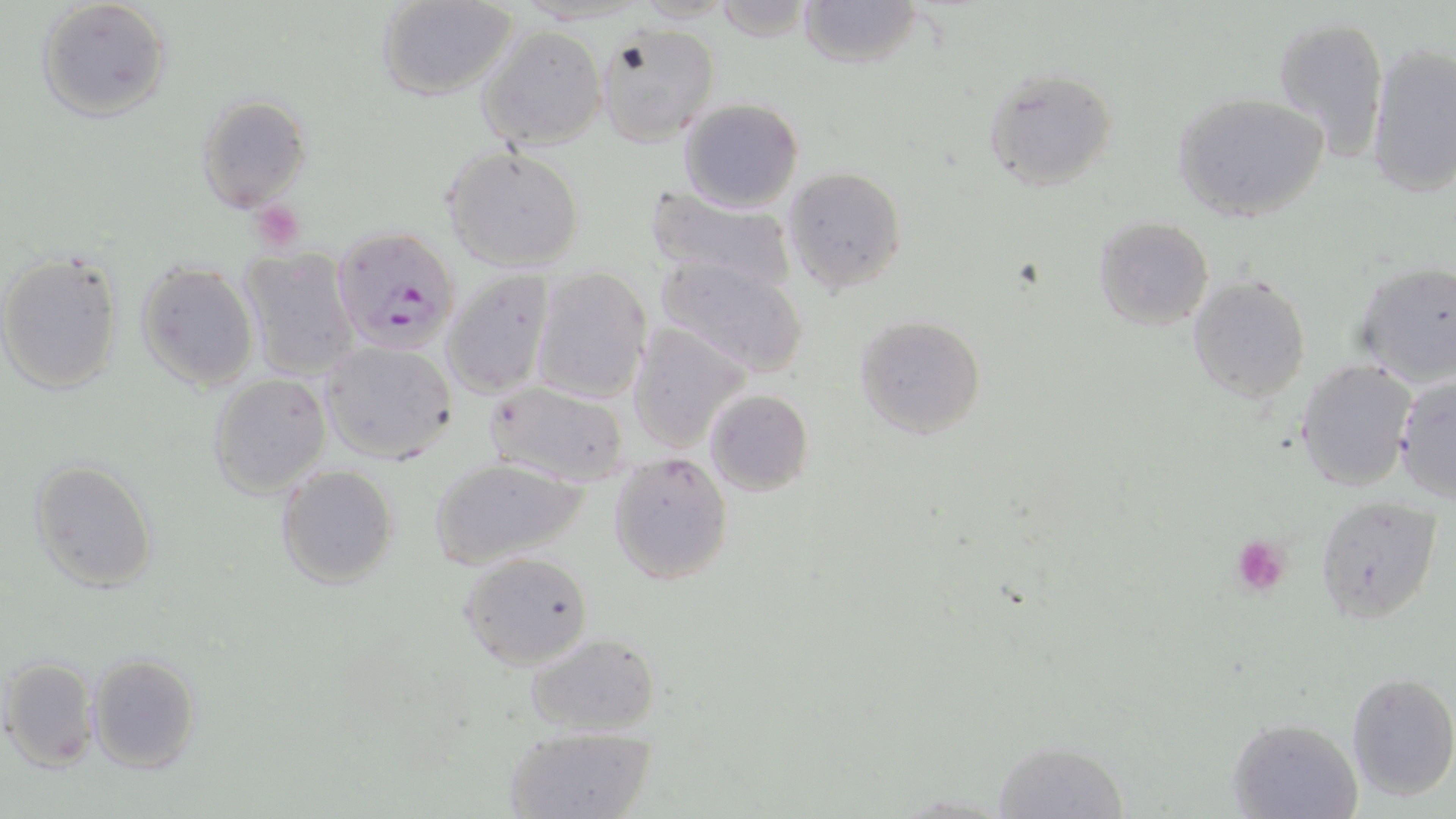
Approximate bounding boxes as named x1/y1/x2/y2 corners in pixels. Uninfected red blood cell locations: (x1=36, y1=0, x2=172, y2=123), (x1=379, y1=0, x2=519, y2=100), (x1=713, y1=0, x2=816, y2=43), (x1=796, y1=0, x2=924, y2=69), (x1=1272, y1=13, x2=1390, y2=162), (x1=594, y1=24, x2=720, y2=148), (x1=478, y1=26, x2=606, y2=150), (x1=1364, y1=41, x2=1456, y2=199), (x1=981, y1=67, x2=1118, y2=193), (x1=1170, y1=91, x2=1331, y2=225), (x1=195, y1=94, x2=312, y2=213), (x1=678, y1=98, x2=805, y2=212), (x1=442, y1=145, x2=586, y2=271), (x1=782, y1=166, x2=908, y2=295), (x1=644, y1=183, x2=797, y2=293), (x1=1093, y1=216, x2=1214, y2=330), (x1=238, y1=248, x2=362, y2=380), (x1=0, y1=250, x2=124, y2=396), (x1=652, y1=254, x2=810, y2=379), (x1=134, y1=260, x2=259, y2=392), (x1=1349, y1=261, x2=1456, y2=387), (x1=442, y1=267, x2=556, y2=398), (x1=530, y1=268, x2=653, y2=402), (x1=1187, y1=274, x2=1311, y2=403), (x1=852, y1=315, x2=988, y2=439), (x1=624, y1=321, x2=749, y2=453), (x1=318, y1=340, x2=460, y2=465), (x1=1295, y1=359, x2=1416, y2=491), (x1=208, y1=372, x2=331, y2=497), (x1=1394, y1=373, x2=1456, y2=501), (x1=483, y1=380, x2=632, y2=487), (x1=704, y1=388, x2=813, y2=497), (x1=607, y1=451, x2=734, y2=584), (x1=428, y1=455, x2=588, y2=570), (x1=30, y1=459, x2=159, y2=593), (x1=276, y1=463, x2=399, y2=589), (x1=1314, y1=494, x2=1443, y2=624), (x1=458, y1=551, x2=593, y2=670), (x1=525, y1=632, x2=662, y2=739), (x1=87, y1=652, x2=200, y2=775), (x1=2, y1=657, x2=101, y2=770), (x1=1345, y1=671, x2=1456, y2=801), (x1=1229, y1=716, x2=1363, y2=819), (x1=502, y1=723, x2=656, y2=818), (x1=989, y1=742, x2=1130, y2=819). Plasmodium falciparum-infected red blood cell locations: (x1=329, y1=226, x2=462, y2=353). Platelet locations: (x1=243, y1=201, x2=303, y2=256), (x1=1230, y1=536, x2=1294, y2=599). Slide-level diagnosis: Plasmodium falciparum. One field of a larger specimen. Captured at 1000x magnification. May-Grünwald-Giemsa stain. Thin blood smear. Image is 1456×819 pixels. Light microscopy.